Report the malaria status of this cell.
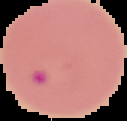
Parasitized.

Image is 127×121 pixels. Segmented cell region on a black background. From a thin blood film.